Assess the morphology of the erythrocytes.
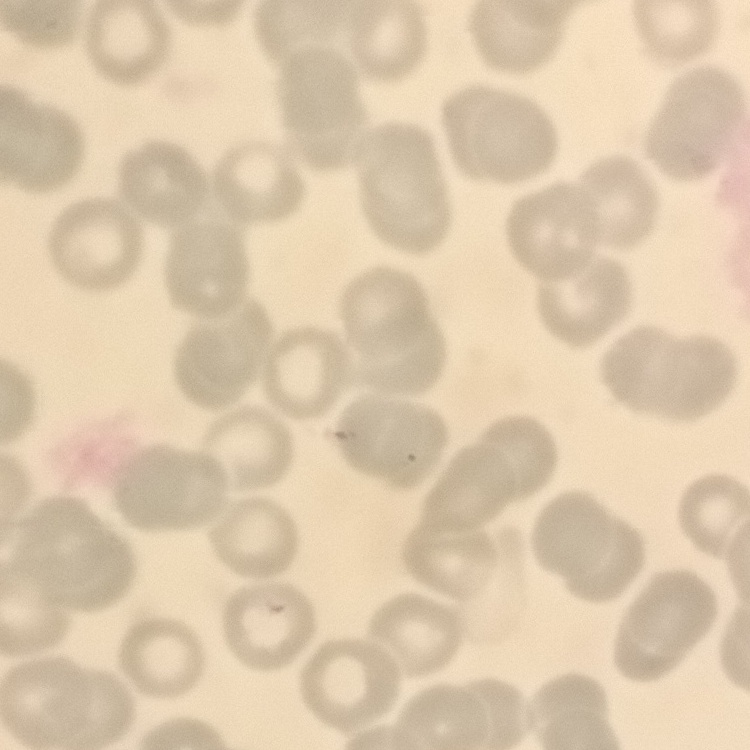

No rouleaux formation.

Square crop of a larger photomicrograph. Field's or Giemsa stain. Thin blood smear.